Report the malaria status of this cell.
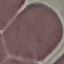

It is uninfected.

Summary:
  - Preparation: thin smear
  - Image type: automatically extracted cell patch, resized to 64 × 64 pixels
  - Stain: Giemsa
  - Capture: smartphone camera at the microscope eyepiece